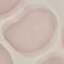 Result: no malaria parasites detected. Giemsa stain. Thin smear of blood. Automatically extracted cell patch, resized to 64 × 64 pixels. Photographed with a smartphone camera at the microscope eyepiece.